Classify this cell by malaria status.
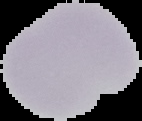

It is uninfected.

image_type: segmented cell region on a black background
image_size: 142×121 pixels
preparation: thin blood film